Report the malaria status of this cell.
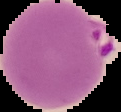

Parasitized.

preparation = thin blood film
image type = cell region segmented out of the field of view; surrounding area masked to black
image size = 121×112 pixels